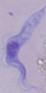
Summary:
  - Magnification: 1000x
  - Modality: micrograph
  - Identification: trypanosome